Comment on the morphology of the red blood cells.
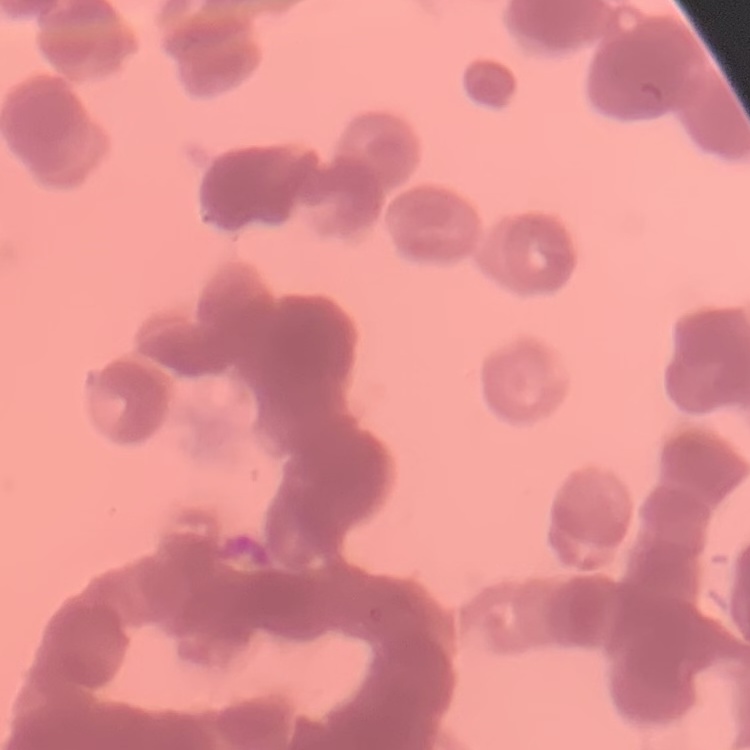
They show rouleaux formation.

One tile cut from a larger photomicrograph. Stained with either Field's or Giemsa. Thin peripheral smear.